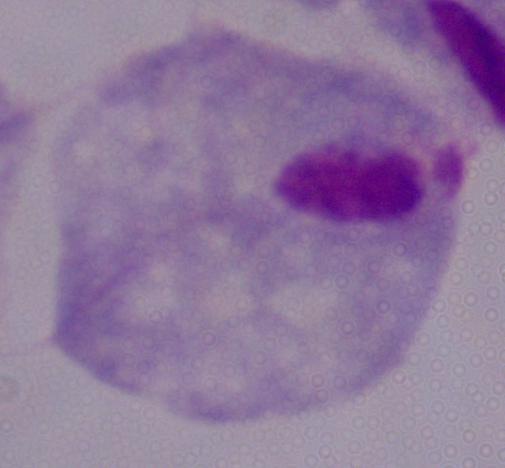 A trichomonad is seen. 1000x magnification. Photomicrograph.